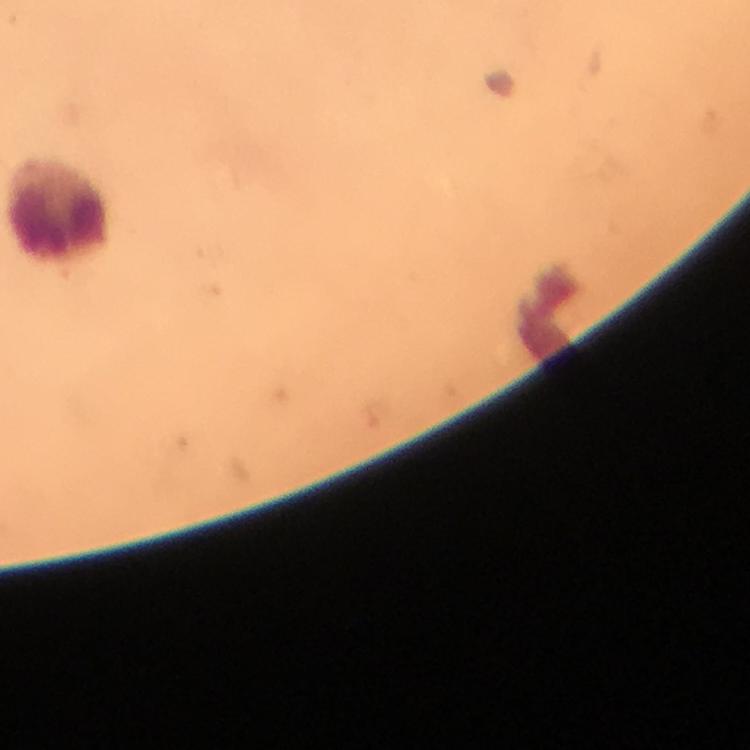

Approximate object centers, in pixels from the top-left corner.
Summary:
  - Leukocyte locations: (x=60, y=213)
  - Image size: 750×750 pixels
  - Preparation: thick blood smear
  - Capture: smartphone mounted on the microscope
  - Cropped from: one field of view
  - Context: from a diagnostic examination for malaria
  - Magnification: 100x
  - Stain: Giemsa
  - Immersion oil: applied
  - Malaria parasites: none seen